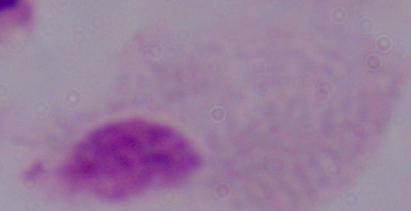
Photomicrograph. A trichomonad is shown. 1000x magnification.